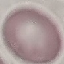 Result: no malaria parasites seen. Photographed with a smartphone camera at the microscope eyepiece. Giemsa-stained preparation. Cell patch, automatically extracted from a larger field of view and resized to 64 × 64 pixels. Thin blood film.